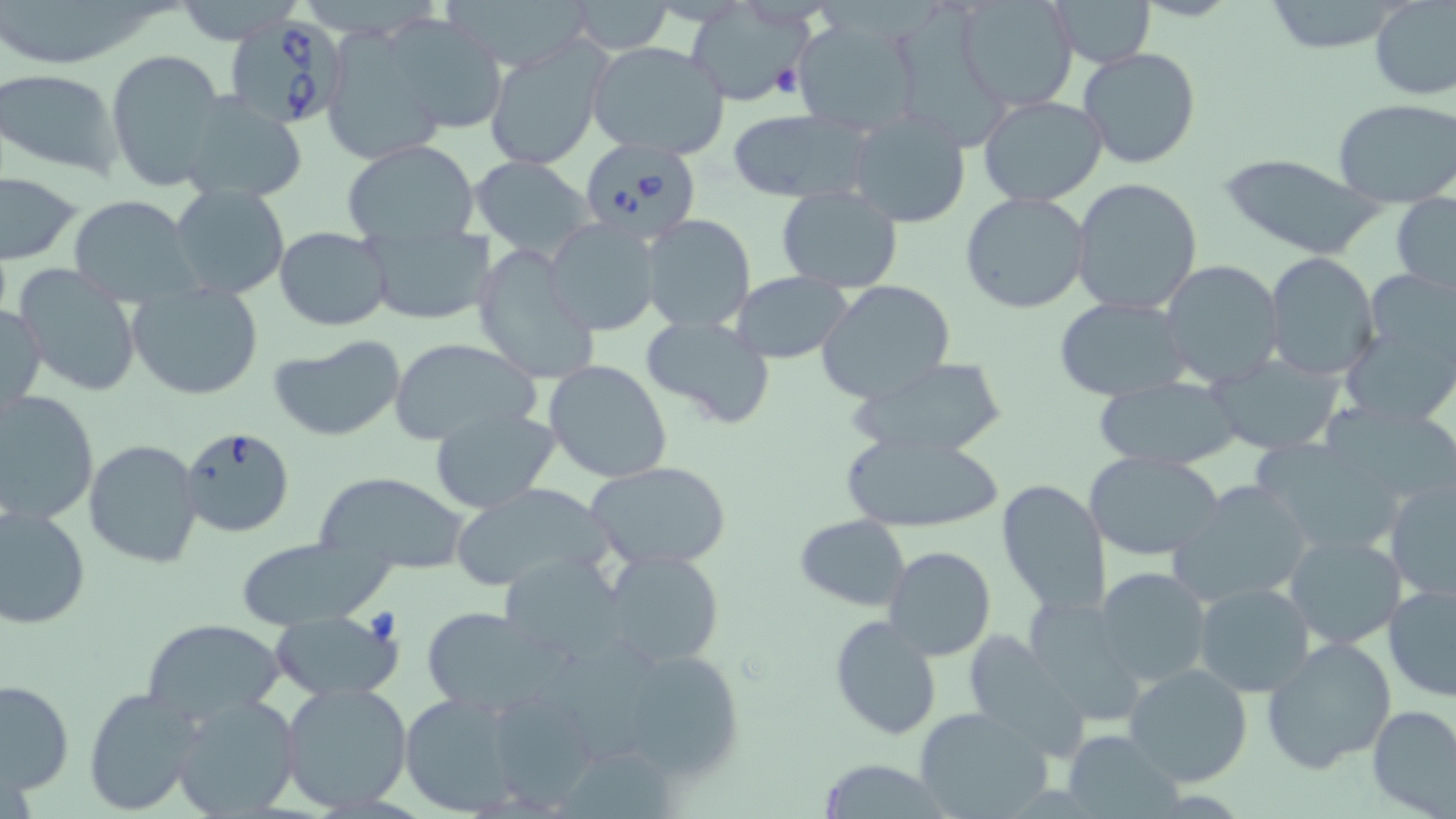

slide_level_diagnosis: Babesia divergens
field_of_view: one of a larger specimen
modality: optical microscopy
preparation: thin blood film
uninfected_red_blood_cell_locations: 'approximate bounding boxes as [x1, y1, x2, y2] in pixels: [172, 0, 304, 44], [953, 0, 1079, 113], [1369, 0, 1456, 101], [570, 1, 673, 54], [1050, 1, 1155, 68], [1255, 1, 1418, 54], [2, 2, 157, 64], [685, 4, 810, 107], [896, 8, 1001, 157], [384, 15, 507, 136], [788, 15, 919, 137], [312, 28, 437, 166], [483, 34, 611, 171], [586, 41, 731, 160], [1078, 47, 1201, 169], [103, 49, 226, 192], [0, 68, 124, 177], [177, 91, 309, 201], [976, 95, 1108, 205], [1334, 99, 1456, 206], [728, 107, 872, 203], [847, 109, 971, 227], [340, 139, 481, 247], [1216, 153, 1385, 261], [469, 155, 595, 259], [1, 172, 85, 266], [1071, 177, 1204, 314], [169, 184, 291, 298], [776, 184, 904, 294], [960, 191, 1090, 314], [1390, 192, 1456, 299], [67, 195, 201, 303], [642, 214, 755, 332], [542, 218, 663, 336], [362, 223, 494, 325], [275, 227, 393, 330], [469, 244, 600, 386], [1263, 252, 1380, 379], [1160, 259, 1287, 391], [11, 268, 145, 398], [731, 271, 850, 364], [815, 279, 956, 406], [128, 284, 264, 401], [1343, 287, 1456, 426], [1054, 297, 1190, 402], [0, 302, 46, 417], [641, 314, 776, 430], [267, 335, 408, 440], [389, 336, 539, 445], [1209, 356, 1342, 453], [544, 358, 673, 483], [851, 358, 1009, 460], [1093, 376, 1247, 471], [0, 390, 99, 525], [1321, 401, 1456, 507], [429, 405, 562, 514], [840, 430, 1005, 532], [82, 438, 203, 569], [1084, 451, 1227, 561], [586, 460, 733, 571], [313, 470, 469, 572], [994, 478, 1110, 617], [1385, 478, 1456, 601], [1169, 479, 1316, 606], [449, 482, 615, 593], [0, 505, 91, 630], [794, 514, 910, 611], [1284, 531, 1408, 650], [232, 539, 389, 630], [883, 545, 996, 661], [601, 548, 726, 668], [500, 553, 628, 661], [1094, 567, 1212, 689], [1383, 581, 1456, 703], [1193, 582, 1317, 699], [1023, 596, 1149, 728], [421, 605, 564, 714], [271, 611, 403, 702], [828, 615, 943, 740], [140, 617, 286, 723], [965, 632, 1088, 752], [554, 635, 678, 768], [1262, 636, 1398, 774], [1123, 663, 1254, 788], [643, 665, 743, 777], [0, 679, 73, 799], [280, 681, 416, 814], [82, 686, 203, 816], [487, 689, 602, 809], [399, 691, 527, 817], [172, 694, 302, 819], [1367, 705, 1456, 817], [914, 706, 1058, 818], [1061, 729, 1184, 818], [815, 759, 953, 818]'
magnification: 1000x
image_size: 1456×819 pixels
babesia_divergens_infected_red_blood_cell_locations: 'approximate bounding boxes as [x1, y1, x2, y2] in pixels: [225, 14, 350, 131], [575, 138, 701, 247], [177, 426, 296, 539]'
stain: May-Grünwald-Giemsa